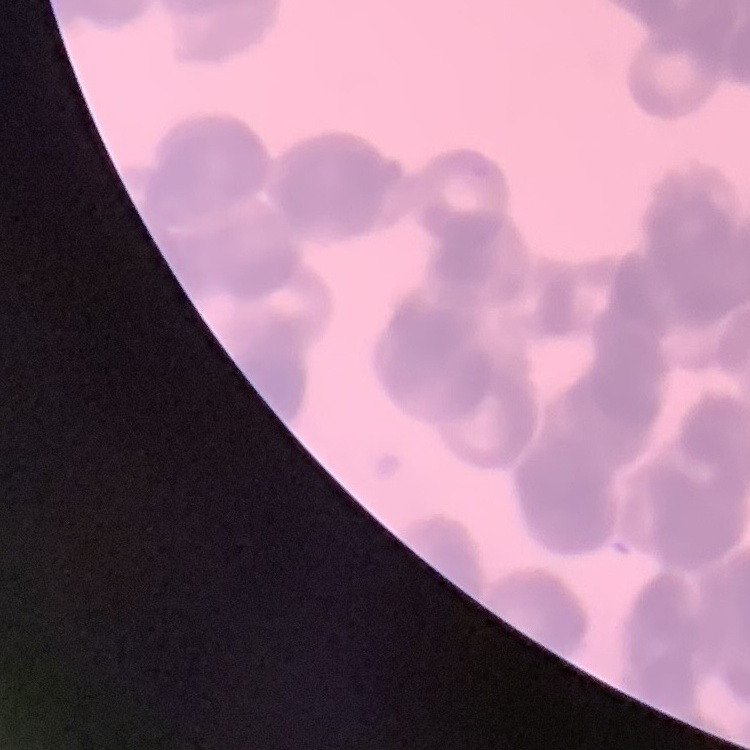 The erythrocytes show rouleaux formation. Thin blood film. Square crop of a larger photomicrograph. Stained with either Field's or Giemsa.